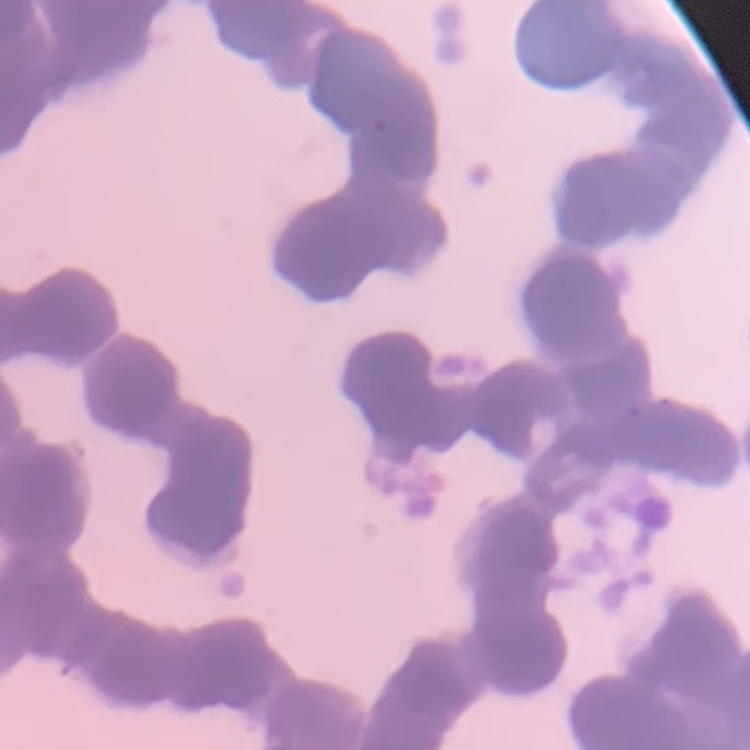
erythrocyte_morphology: rouleaux formation
stain: Field's or Giemsa
image_type: square crop of a larger photomicrograph
preparation: thin blood smear